Classify this cell by malaria status.
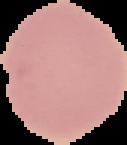
Uninfected.

From a thin blood smear. The area outside the segmented cell region is set to black. Image is 127×145 pixels.